Give the position of every Plasmodium parasite visible.
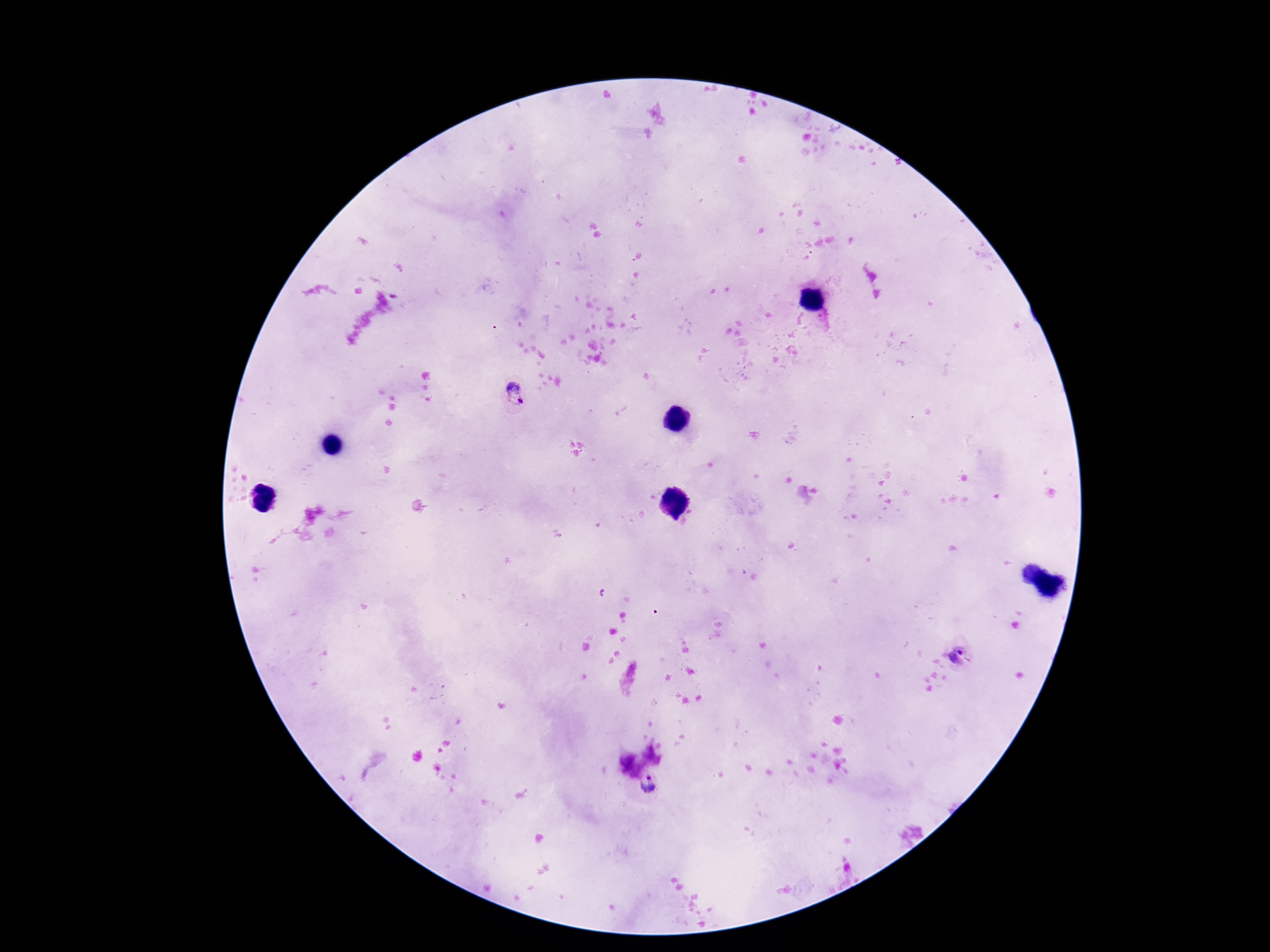
Approximate centers as {x, y} in pixels.
Plasmodium parasites: {516, 395}, {959, 654}, {648, 786}.

Summary:
  - Field of view: one from this slide
  - Patient malaria status: infected
  - Capture: smartphone camera through the microscope eyepiece
  - Magnification: 100x
  - Stain: Giemsa
  - Image size: 1270×952 pixels
  - Preparation: thick blood smear